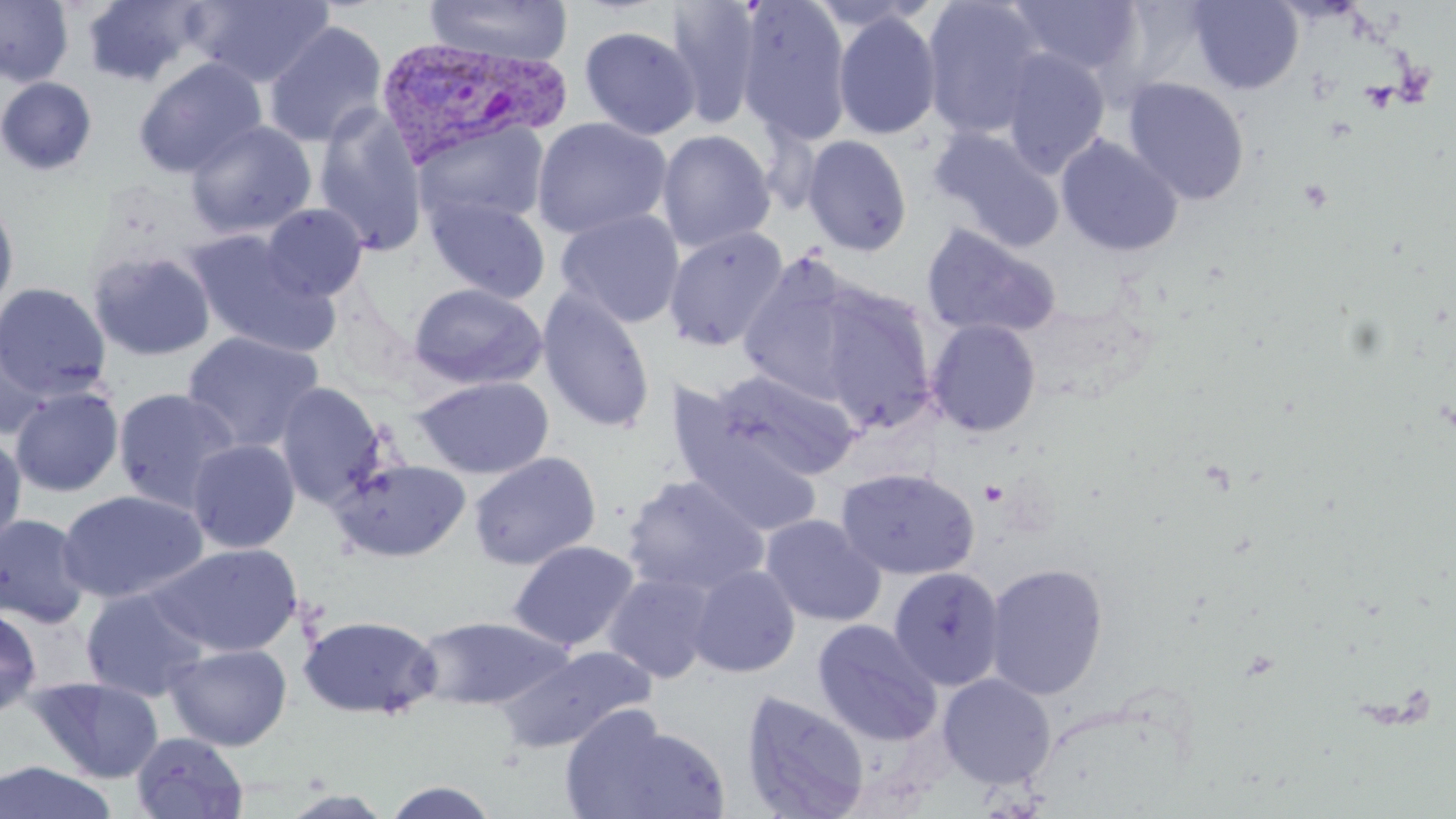

slide_level_diagnosis: Plasmodium vivax
uninfected_red_blood_cell_locations: 'approximate bounding boxes as named x1/y1/x2/y2 corners in pixels: (x1=0, y1=0, x2=73, y2=87), (x1=81, y1=0, x2=207, y2=87), (x1=190, y1=0, x2=335, y2=88), (x1=423, y1=0, x2=573, y2=66), (x1=663, y1=0, x2=763, y2=127), (x1=738, y1=0, x2=853, y2=146), (x1=921, y1=0, x2=1047, y2=140), (x1=1187, y1=0, x2=1304, y2=95), (x1=1005, y1=1, x2=1145, y2=80), (x1=833, y1=11, x2=942, y2=141), (x1=264, y1=22, x2=388, y2=148), (x1=579, y1=24, x2=700, y2=140), (x1=1000, y1=49, x2=1110, y2=176), (x1=134, y1=57, x2=267, y2=178), (x1=0, y1=76, x2=98, y2=176), (x1=1123, y1=78, x2=1250, y2=206), (x1=313, y1=105, x2=429, y2=257), (x1=531, y1=116, x2=672, y2=240), (x1=414, y1=119, x2=551, y2=232), (x1=186, y1=120, x2=316, y2=238), (x1=929, y1=127, x2=1064, y2=251), (x1=656, y1=129, x2=776, y2=254), (x1=1056, y1=134, x2=1184, y2=257), (x1=802, y1=135, x2=913, y2=256), (x1=425, y1=192, x2=551, y2=304), (x1=0, y1=195, x2=19, y2=318), (x1=260, y1=203, x2=369, y2=302), (x1=556, y1=208, x2=685, y2=328), (x1=921, y1=224, x2=1062, y2=340), (x1=664, y1=226, x2=790, y2=352), (x1=187, y1=230, x2=340, y2=358), (x1=88, y1=249, x2=216, y2=362), (x1=736, y1=257, x2=873, y2=405), (x1=0, y1=281, x2=111, y2=400), (x1=408, y1=282, x2=547, y2=391), (x1=818, y1=286, x2=937, y2=432), (x1=536, y1=288, x2=656, y2=434), (x1=926, y1=318, x2=1042, y2=438), (x1=182, y1=331, x2=325, y2=452), (x1=1, y1=335, x2=55, y2=439), (x1=712, y1=369, x2=862, y2=481), (x1=413, y1=375, x2=554, y2=479), (x1=275, y1=383, x2=388, y2=509), (x1=9, y1=386, x2=124, y2=497), (x1=112, y1=387, x2=242, y2=513), (x1=675, y1=427, x2=823, y2=537), (x1=0, y1=432, x2=27, y2=552), (x1=186, y1=439, x2=300, y2=554), (x1=467, y1=451, x2=601, y2=570), (x1=331, y1=457, x2=471, y2=562), (x1=837, y1=466, x2=980, y2=580), (x1=621, y1=475, x2=769, y2=597), (x1=56, y1=489, x2=209, y2=604), (x1=0, y1=513, x2=92, y2=628), (x1=760, y1=513, x2=886, y2=627), (x1=508, y1=540, x2=639, y2=652), (x1=148, y1=543, x2=302, y2=657), (x1=985, y1=562, x2=1108, y2=701), (x1=688, y1=565, x2=800, y2=678), (x1=887, y1=567, x2=1005, y2=690), (x1=604, y1=571, x2=718, y2=683), (x1=81, y1=587, x2=210, y2=701), (x1=0, y1=606, x2=42, y2=718), (x1=298, y1=614, x2=443, y2=720), (x1=413, y1=615, x2=575, y2=710), (x1=812, y1=619, x2=942, y2=745), (x1=163, y1=642, x2=293, y2=750), (x1=494, y1=645, x2=654, y2=754), (x1=937, y1=673, x2=1056, y2=790), (x1=28, y1=675, x2=164, y2=783), (x1=741, y1=691, x2=870, y2=819), (x1=562, y1=710, x2=732, y2=819), (x1=129, y1=732, x2=249, y2=818), (x1=0, y1=761, x2=120, y2=819), (x1=381, y1=780, x2=500, y2=818), (x1=280, y1=789, x2=396, y2=818)'
preparation: thin blood smear
modality: light microscopy
image_size: 1456×819 pixels
field_of_view: one of a larger specimen
platelet_locations: 'approximate bounding boxes as named x1/y1/x2/y2 corners in pixels: (x1=1358, y1=83, x2=1398, y2=112), (x1=1298, y1=178, x2=1334, y2=214), (x1=979, y1=480, x2=1009, y2=508)'
plasmodium_vivax_infected_red_blood_cell_locations: 'approximate bounding boxes as named x1/y1/x2/y2 corners in pixels: (x1=371, y1=36, x2=570, y2=168)'
stain: May-Grünwald-Giemsa
magnification: 1000x